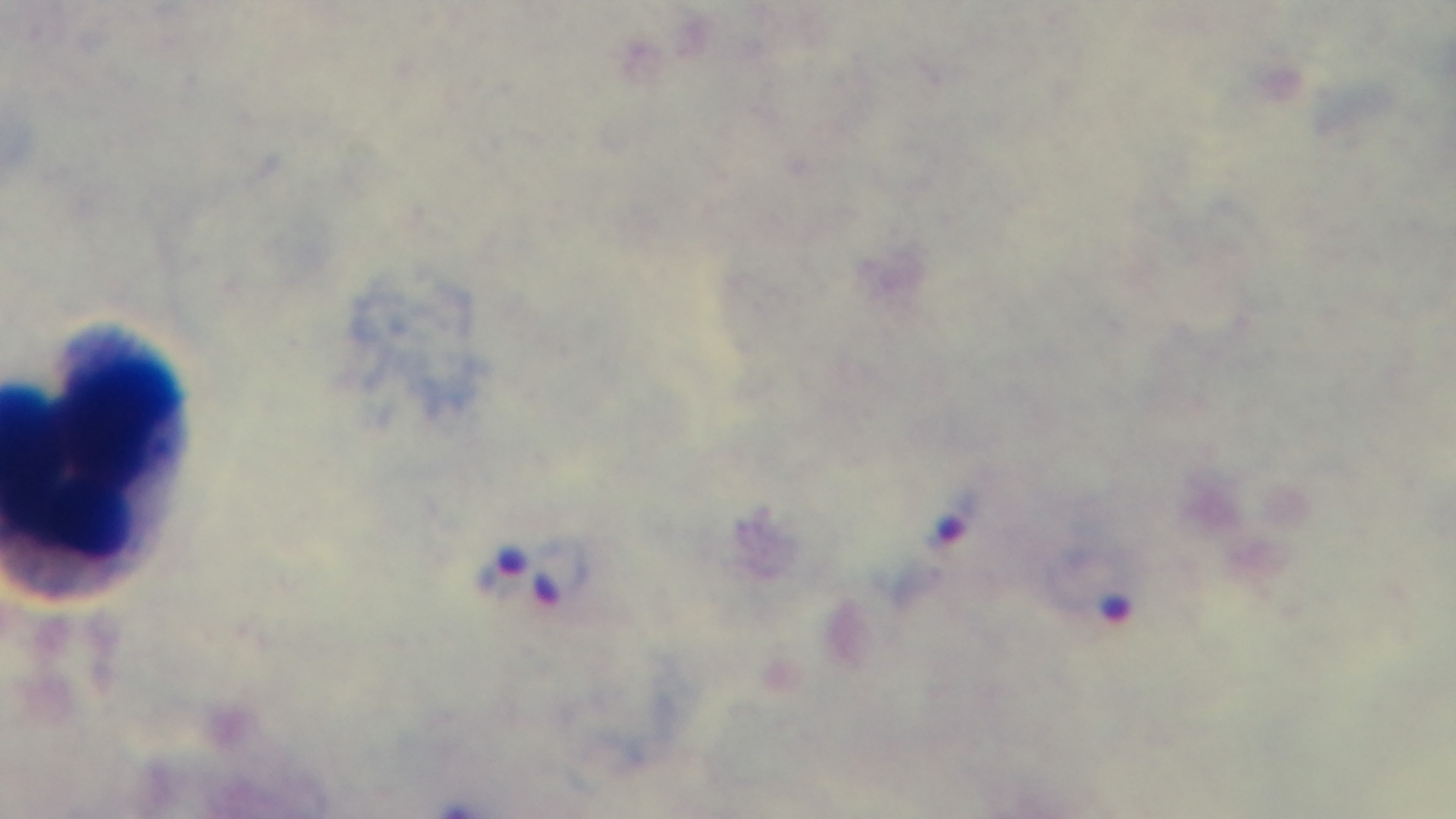
malaria status = infected
preparation = thick blood film
stain = Giemsa
field of view = one from the slide
objective = 100x oil immersion
modality = light microscopy
capture = mounted 4K digital camera